Assess this cell for malaria.
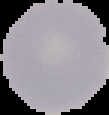
Uninfected.

The area outside the segmented cell region is set to black. From a thin blood film. Image is 109×115 pixels.